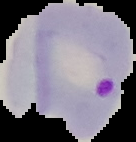

image_type: segmented cell region with the area outside set to black
preparation: thin blood film
image_size: 136×142 pixels
result: malaria parasites detected